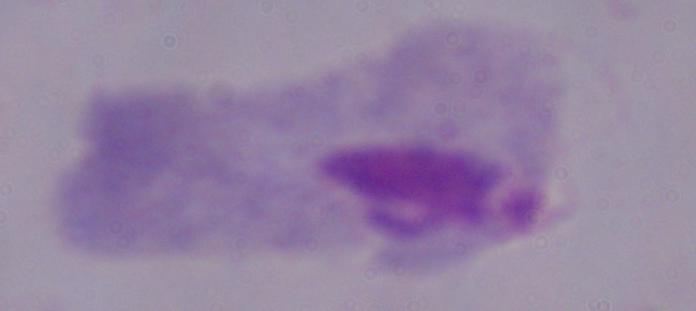

Summary:
  - Identification: trichomonad
  - Magnification: 1000x
  - Modality: micrograph